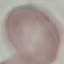
result = no malaria parasites detected
preparation = thin blood smear
image type = cell patch, automatically extracted from a larger field of view and resized to 64 × 64 pixels
stain = Giemsa
capture = smartphone through the microscope eyepiece